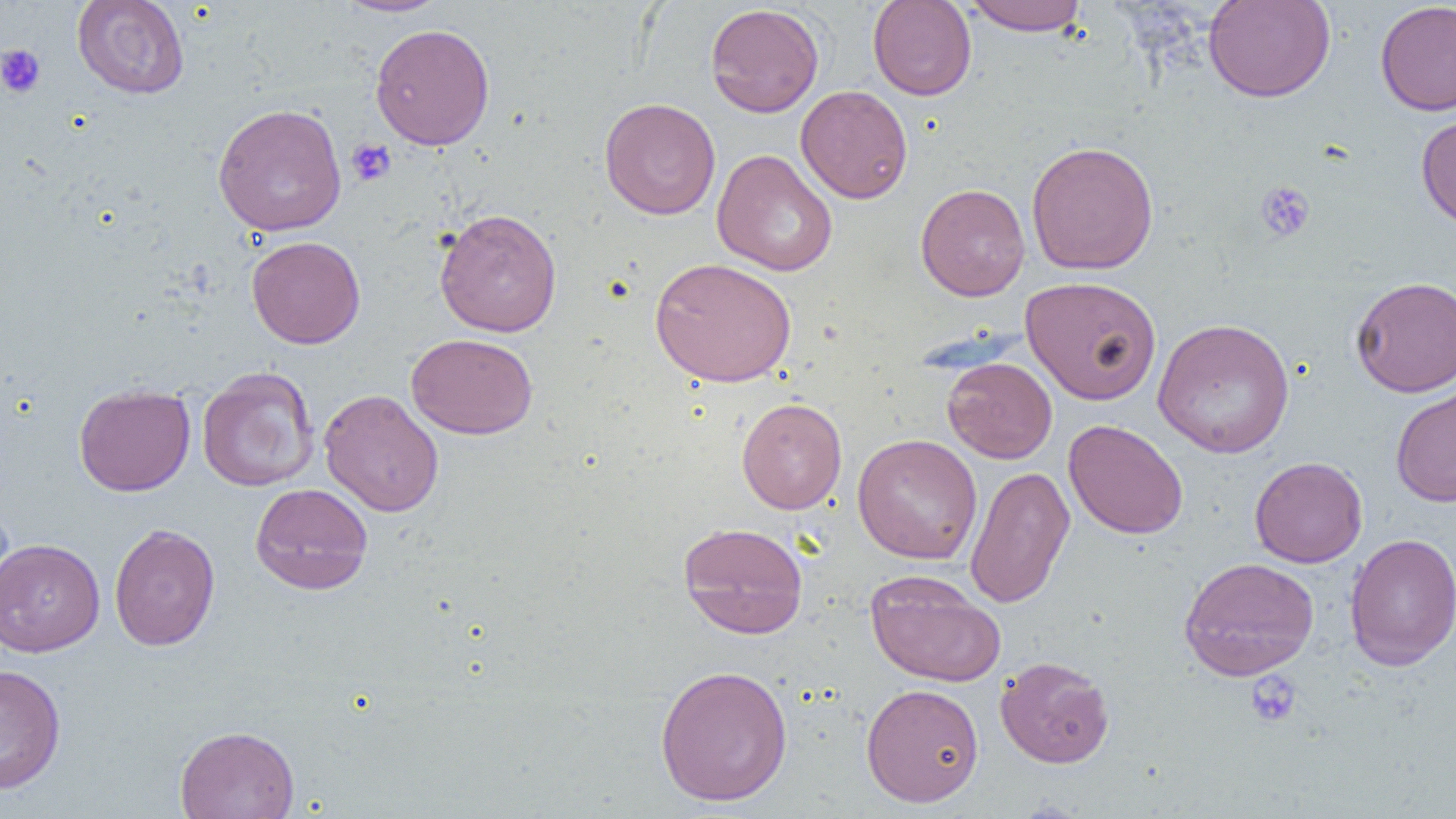

{
  "slide_level_diagnosis": "negative for blood parasites",
  "modality": "optical microscopy",
  "preparation": "thin blood film",
  "field_of_view": "single",
  "uninfected_red_blood_cell_locations": "approximate bounding boxes as (x1, y1, x2, y2) in pixels: (72, 0, 190, 99), (334, 0, 450, 17), (867, 0, 977, 100), (961, 0, 1090, 35), (1203, 0, 1336, 103), (1375, 2, 1456, 116), (705, 3, 824, 117), (370, 23, 495, 150), (796, 85, 913, 204), (599, 97, 720, 219), (213, 103, 347, 237), (1416, 111, 1456, 230), (1026, 140, 1159, 276), (712, 149, 838, 276), (915, 183, 1030, 301), (434, 207, 563, 337), (246, 235, 366, 349), (650, 257, 797, 388), (1021, 276, 1161, 405), (1350, 276, 1456, 396), (1153, 317, 1294, 459), (406, 333, 538, 439), (942, 357, 1057, 463), (197, 366, 319, 492), (73, 383, 195, 496), (1390, 383, 1456, 507), (319, 389, 444, 517), (736, 398, 847, 514), (1063, 419, 1188, 540), (852, 433, 982, 564), (1250, 456, 1367, 568), (965, 465, 1075, 609), (250, 482, 373, 595), (678, 521, 809, 638), (108, 523, 220, 651), (1344, 533, 1456, 671), (0, 537, 104, 657), (1178, 556, 1319, 681), (865, 570, 1006, 687), (995, 655, 1115, 768), (654, 663, 793, 807), (0, 664, 66, 794), (861, 682, 984, 807), (174, 725, 300, 819)",
  "magnification": "1000x",
  "image_size": "1456×819 pixels",
  "platelet_locations": "approximate bounding boxes as (x1, y1, x2, y2) in pixels: (0, 44, 46, 98), (346, 138, 397, 187), (1255, 180, 1315, 241), (1245, 671, 1302, 727)"
}